Point out each malaria parasite.
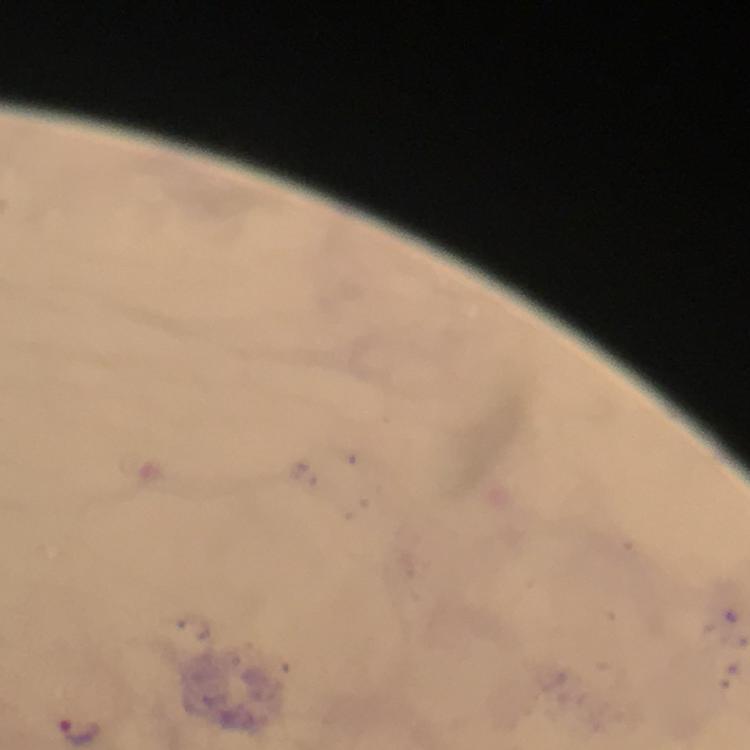
Approximate centers as {x, y} in pixels.
Malaria parasites: {81, 730}.

Summary:
  - Context: from a malaria diagnostic workup
  - Preparation: thick blood smear
  - Cropped from: one field of view
  - Immersion oil: used
  - Magnification: 100x
  - Stain: Giemsa
  - Image size: 750×750 pixels
  - Capture: smartphone mounted on the microscope